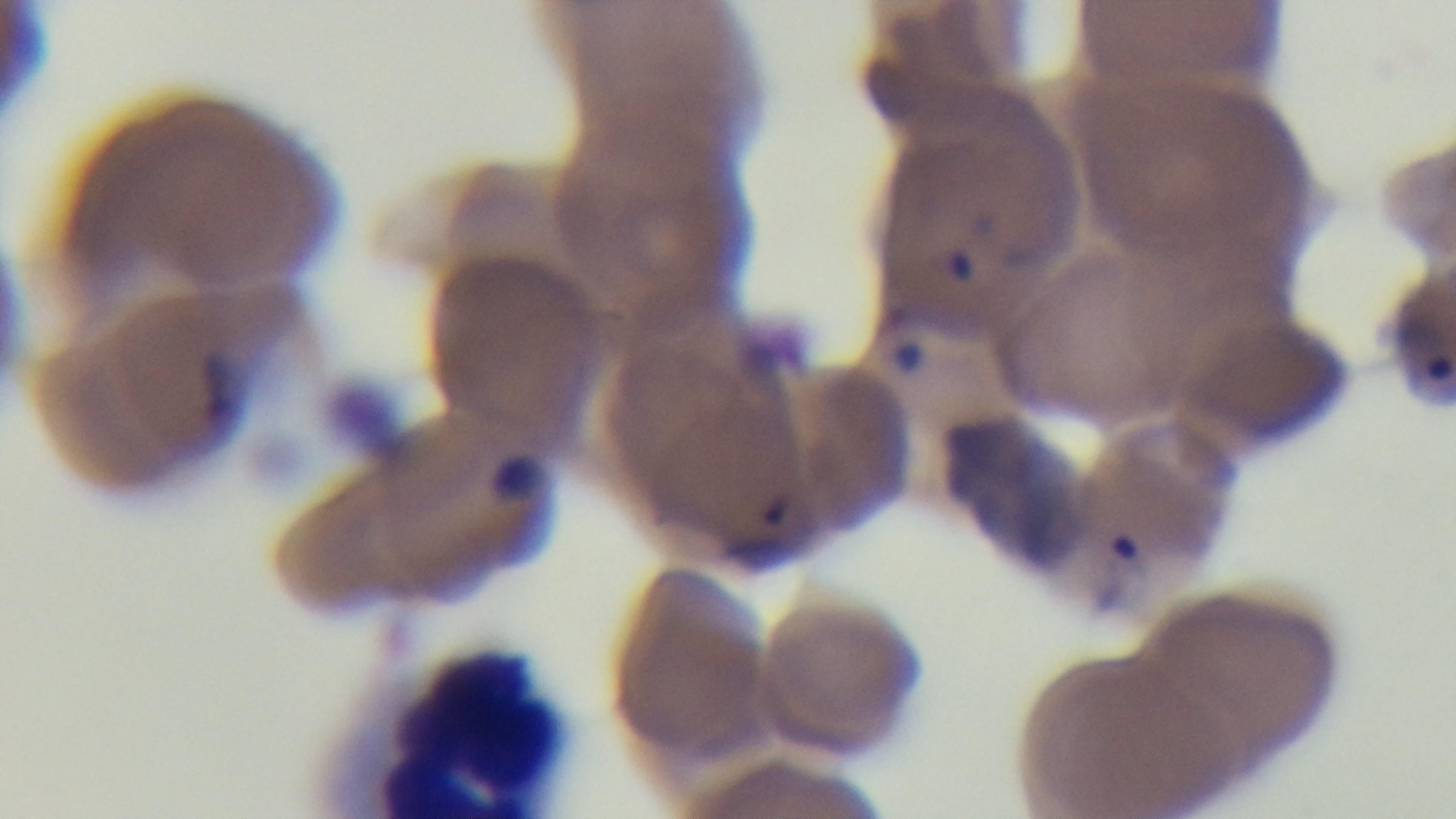
field of view = one from the slide
modality = light microscopy
malaria status = positive
stain = Giemsa
preparation = thin blood film
capture = mounted 4K digital camera
objective = 100x oil immersion